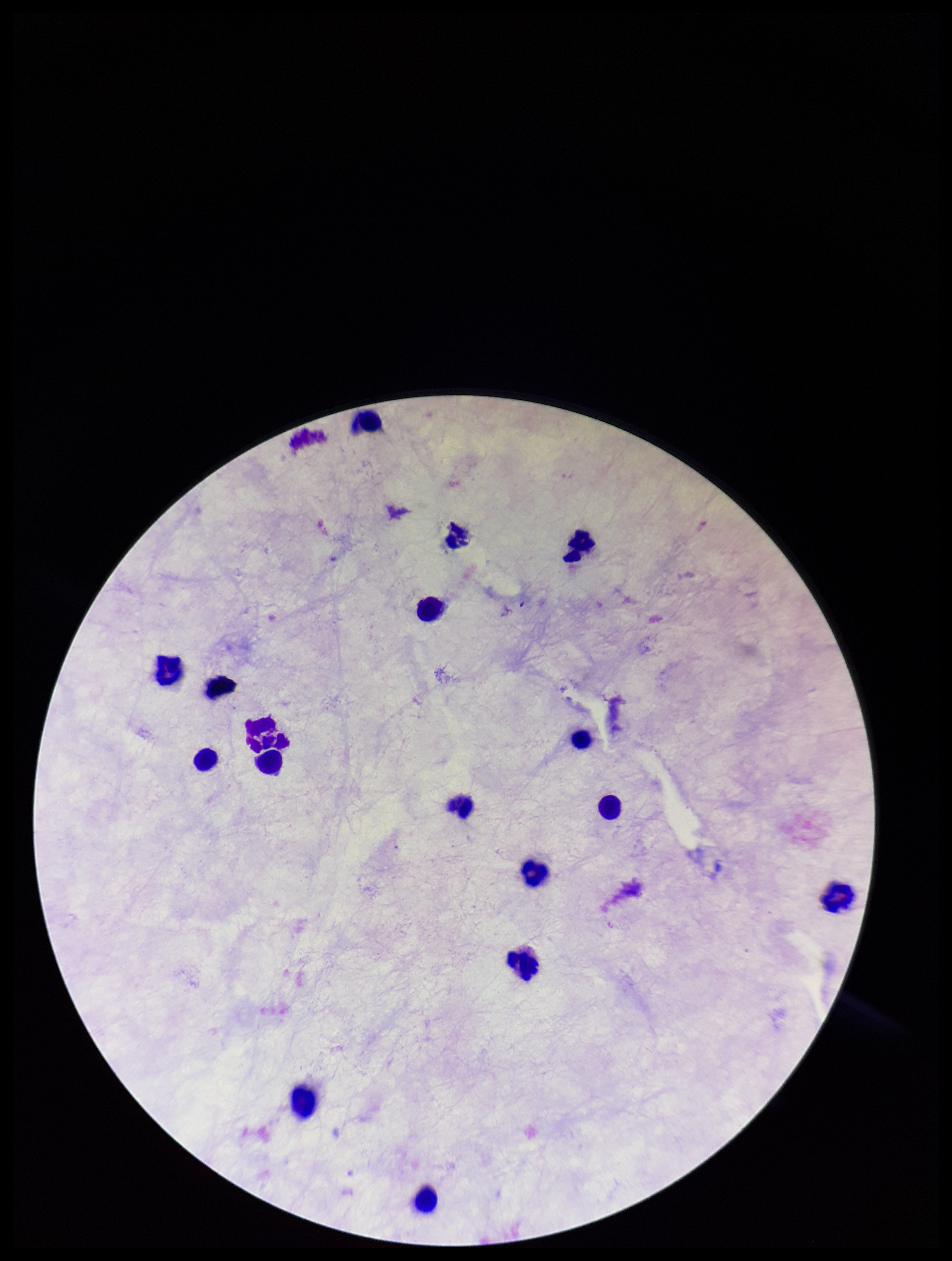
Summary:
  - Preparation: thick smear
  - Patient malaria status: negative
  - Capture: smartphone photograph through the microscope eyepiece
  - Image size: 952×1261 pixels
  - Plasmodium parasites: none identified
  - Field of view: one from this slide
  - Parasite count: 0
  - Stain: Giemsa
  - Leukocyte count: 16